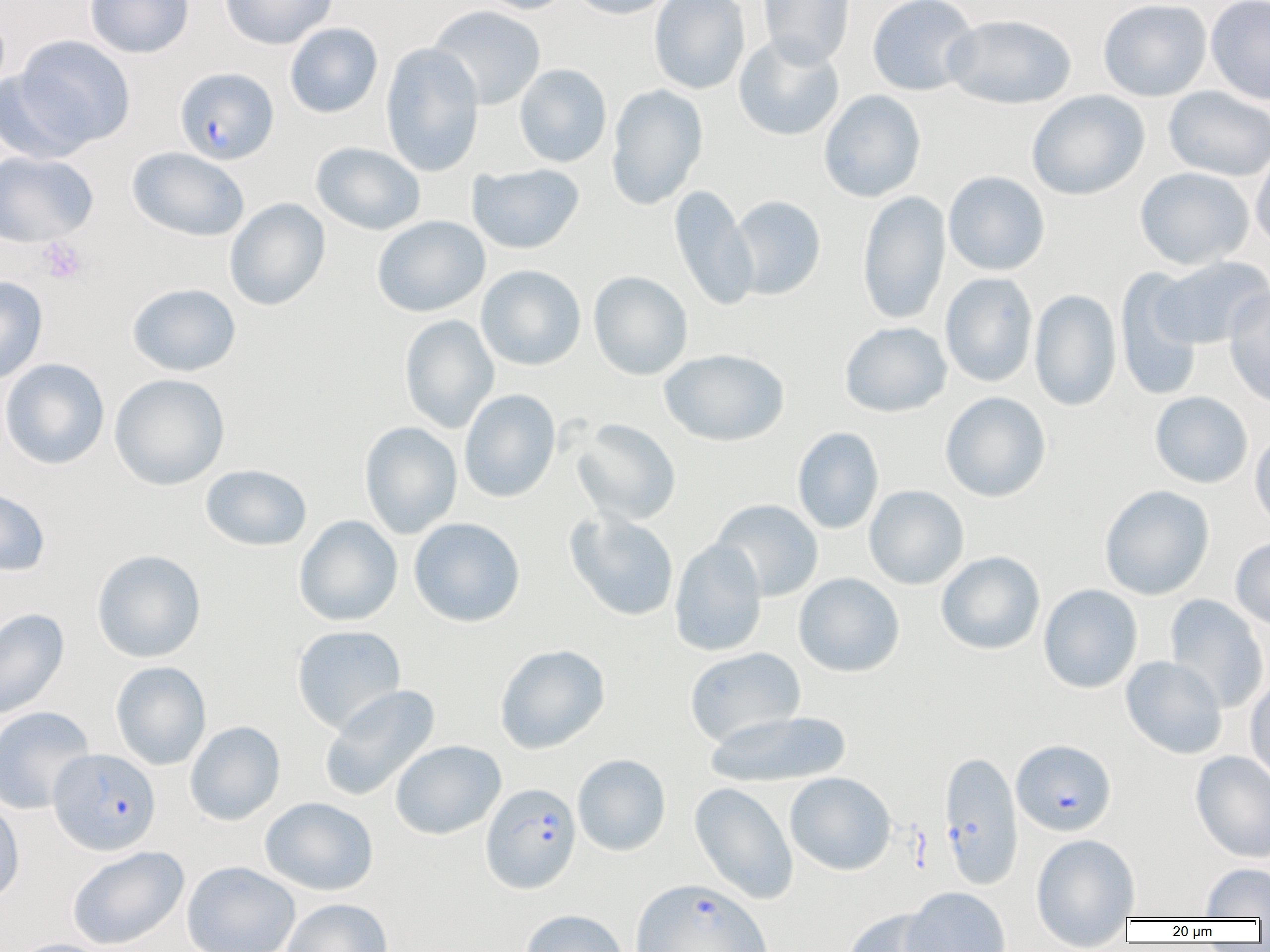
Plasmodium falciparum-infected red blood cell locations = approximate bounding boxes as [x1, y1, x2, y2] in pixels: [174, 66, 279, 164], [1011, 739, 1116, 836], [48, 748, 161, 855], [938, 750, 1024, 889], [480, 782, 581, 894], [630, 877, 773, 952]
slide-level diagnosis = Plasmodium falciparum
uninfected red blood cell locations = approximate bounding boxes as [x1, y1, x2, y2] in pixels: [84, 0, 194, 58], [220, 0, 337, 50], [473, 0, 576, 14], [569, 0, 676, 19], [648, 0, 751, 94], [757, 0, 856, 67], [867, 0, 979, 97], [1098, 0, 1212, 101], [1206, 0, 1270, 105], [427, 5, 546, 110], [944, 14, 1077, 109], [284, 22, 383, 118], [733, 34, 845, 141], [12, 35, 136, 150], [380, 42, 484, 177], [514, 64, 612, 168], [0, 67, 95, 163], [606, 84, 708, 210], [1163, 86, 1270, 182], [818, 89, 926, 202], [1027, 90, 1149, 200], [310, 142, 425, 235], [127, 147, 249, 241], [1251, 147, 1270, 253], [0, 150, 98, 246], [467, 163, 585, 254], [1135, 166, 1255, 270], [943, 171, 1051, 276], [669, 185, 758, 312], [856, 190, 951, 326], [728, 195, 826, 300], [224, 198, 330, 311], [372, 215, 490, 317], [1151, 257, 1270, 349], [476, 265, 586, 371], [1115, 269, 1204, 401], [588, 271, 693, 380], [939, 272, 1038, 387], [0, 275, 48, 384], [127, 283, 241, 377], [1224, 287, 1270, 408], [1029, 289, 1122, 411], [399, 315, 500, 433], [839, 321, 952, 417], [660, 348, 790, 446], [0, 358, 110, 469], [109, 373, 230, 490], [459, 389, 561, 503], [1150, 391, 1253, 489], [940, 392, 1052, 502], [572, 418, 682, 525], [359, 421, 462, 539], [792, 426, 884, 534], [1250, 429, 1270, 532], [200, 464, 312, 552], [0, 485, 51, 577], [864, 485, 969, 590], [1100, 485, 1214, 600], [710, 499, 824, 601], [564, 510, 679, 621], [294, 515, 403, 626], [409, 517, 526, 627], [1230, 536, 1270, 631], [669, 539, 767, 657], [92, 549, 206, 662], [936, 551, 1045, 655], [793, 572, 905, 677], [1038, 584, 1143, 694], [1164, 594, 1269, 713], [0, 608, 69, 719], [291, 625, 406, 734], [494, 644, 610, 754], [684, 647, 805, 748], [1120, 656, 1228, 759], [110, 661, 211, 770], [1245, 676, 1270, 785], [318, 685, 440, 802], [0, 706, 95, 814], [705, 709, 853, 789], [185, 720, 285, 825], [390, 740, 506, 840], [1190, 750, 1270, 863], [572, 754, 671, 856], [785, 772, 896, 876], [689, 782, 798, 905], [260, 796, 379, 896], [0, 798, 25, 907], [1030, 832, 1141, 949], [66, 846, 189, 950], [181, 860, 300, 952], [1200, 862, 1269, 919], [900, 886, 1011, 952], [282, 898, 393, 952], [843, 907, 948, 952], [520, 909, 629, 952], [8, 938, 113, 952]
preparation = thin blood smear
modality = light microscopy
magnification = 1000x
image size = 1270×952 pixels
field of view = single
platelet locations = approximate bounding boxes as [x1, y1, x2, y2] in pixels: [37, 238, 88, 284]